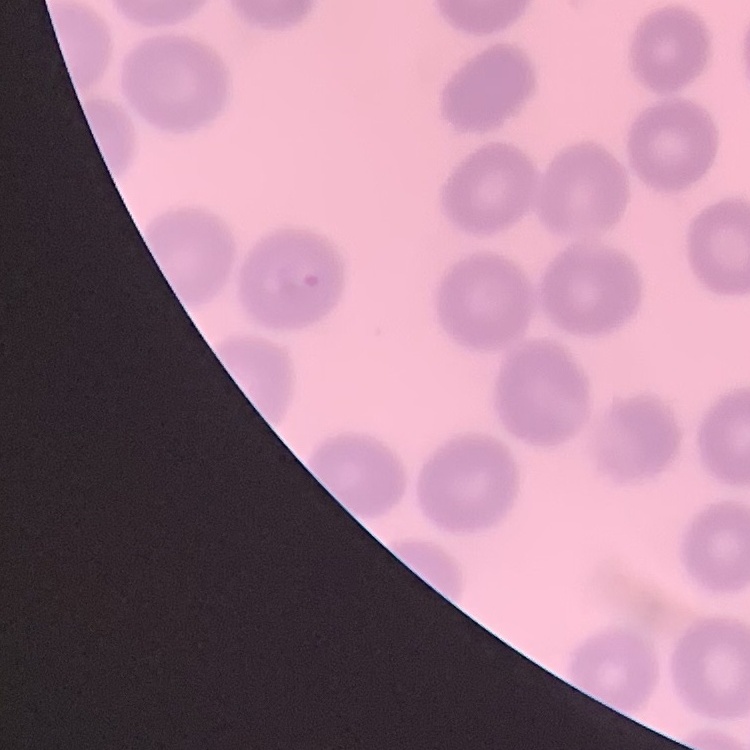
Summary:
  - Red blood cell morphology: no rouleaux formation
  - Stain: Field's or Giemsa
  - Image type: one tile cut from a larger photomicrograph
  - Preparation: thin blood smear